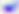

Summary:
  - Magnification: 400x
  - Identification: Toxoplasma gondii
  - Modality: photomicrograph